Comment on the morphology of the red blood cells.
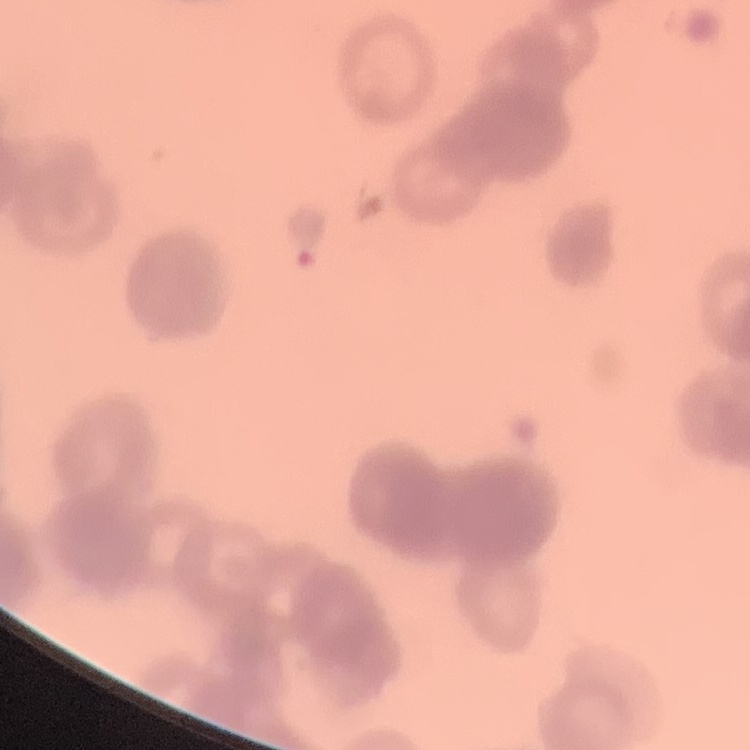

Rouleaux formation.

Thin blood film. Field's or Giemsa stain. Square crop of a larger photomicrograph.